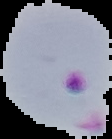

Malaria status: parasitized. From a thin blood film. Image is 112×139 pixels. Segmented cell region on a black background.